Comment on the background quality.
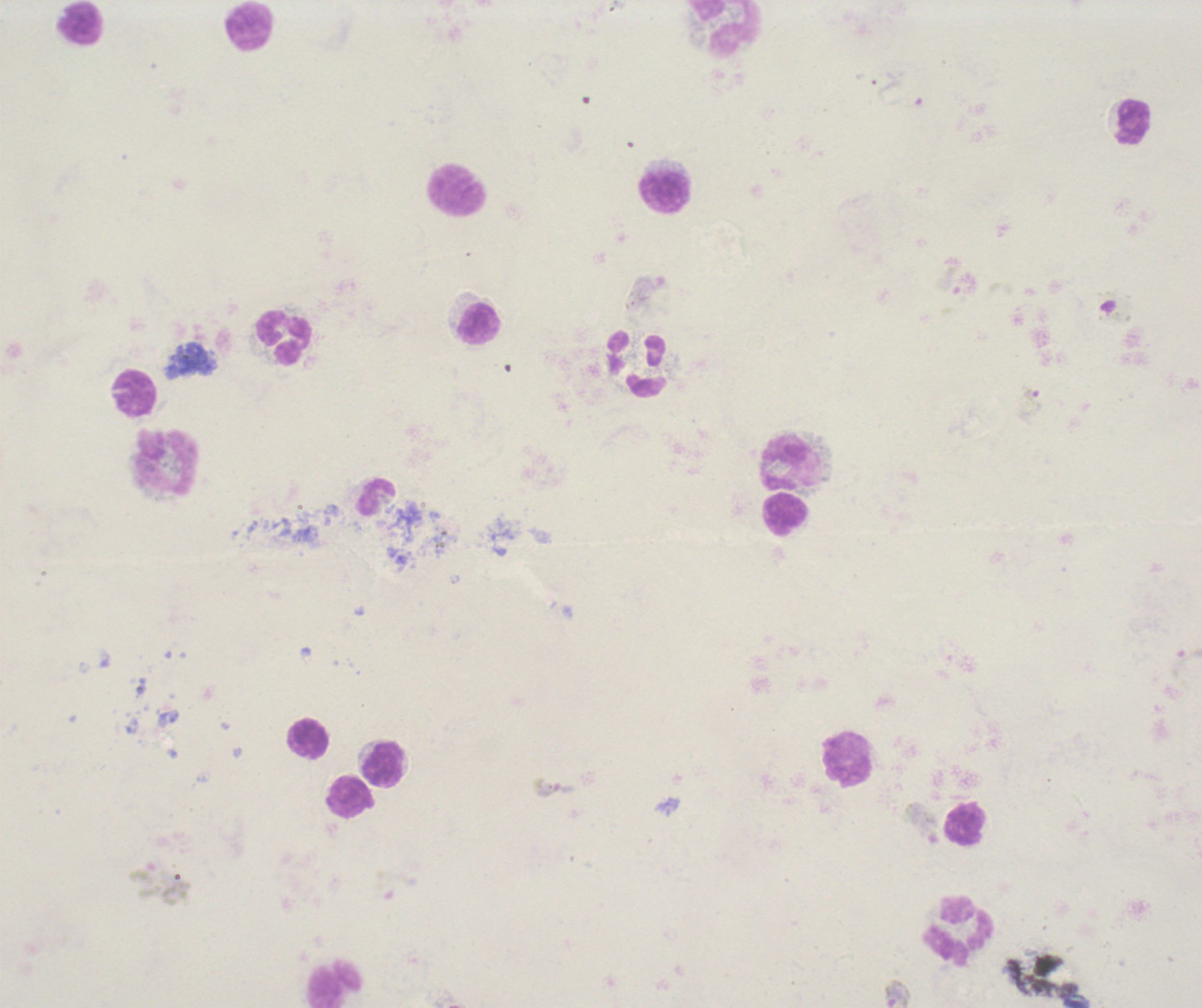
Poor.

Approximate object centers, in pixels from the top-left corner. Gametocyte locations: (x=1115, y=305), (x=923, y=823), (x=897, y=994). Leukocyte locations: (x=82, y=23), (x=250, y=28), (x=727, y=28), (x=1135, y=122), (x=458, y=191), (x=665, y=192), (x=479, y=324), (x=284, y=337), (x=636, y=365), (x=135, y=395), (x=167, y=461), (x=791, y=463), (x=376, y=497), (x=786, y=514), (x=310, y=740), (x=848, y=759), (x=383, y=764), (x=352, y=798), (x=965, y=824), (x=960, y=931), (x=336, y=984). Trophozoite locations: (x=1032, y=401), (x=1185, y=667), (x=555, y=788). Life-cycle stages observed: trophozoite, gametocyte. Thick smear of blood. Single field of view. Romanowsky-stained preparation. Coloration quality: bad. Captured at 100x magnification. Previously used in an actual diagnosis. Result: positive for malaria parasites. Image is 1202×1008 pixels.